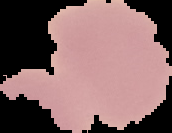
Segmented cell region on a black background. From a thin blood film. Image is 172×133 pixels. Result: no malaria parasites seen.